Identify the parasite.
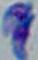

This is Toxoplasma gondii.

magnification: 1000x
modality: photomicrograph